Assess this cell for malaria.
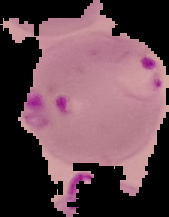
Parasitized.

Image is 169×217 pixels. The area outside the segmented cell region is set to black. From a thin blood film.